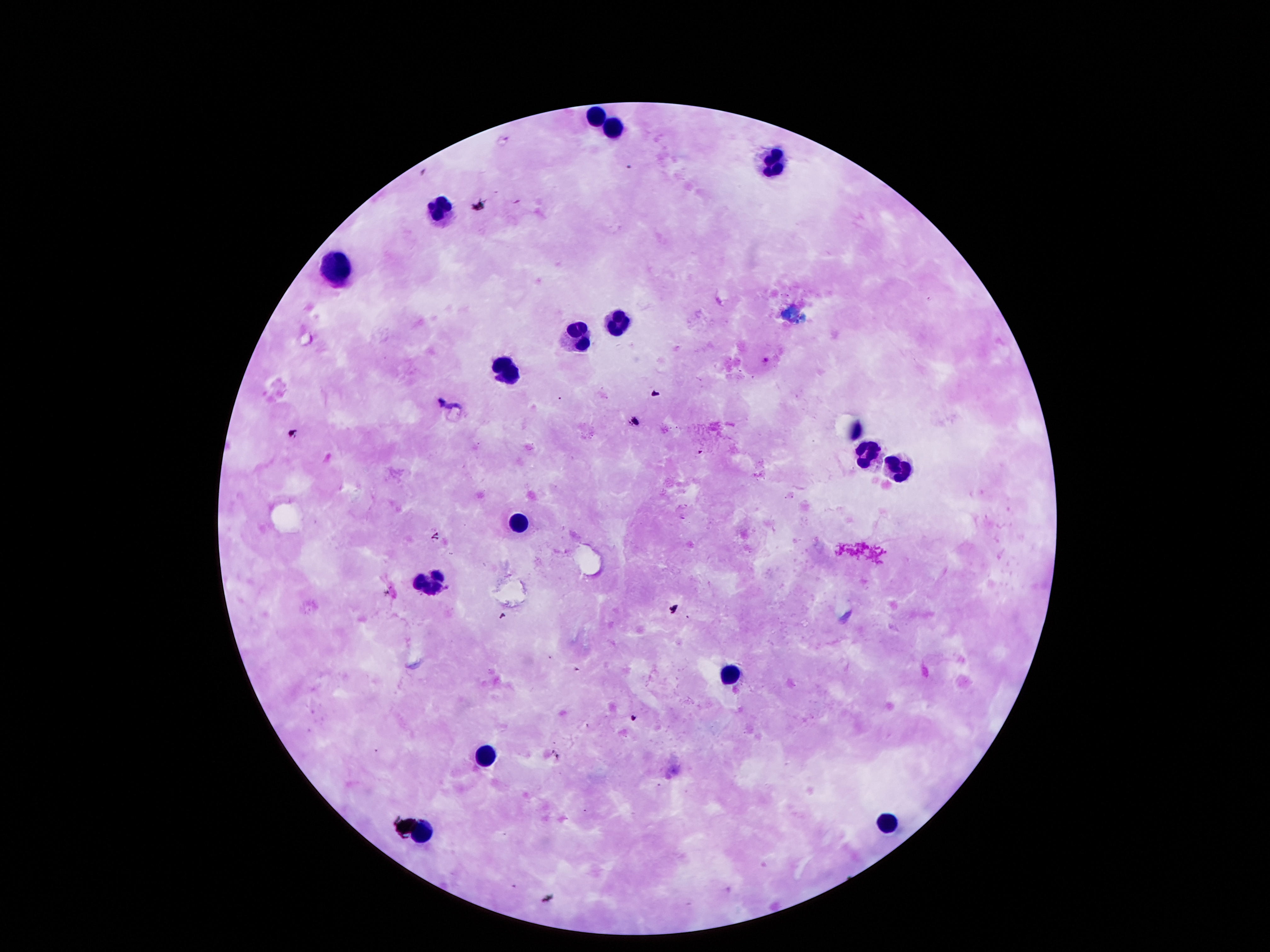
Approximate centers as {x, y} in pixels.
Summary:
  - Leukocyte locations: {593, 113}, {613, 127}, {778, 162}, {440, 211}, {338, 267}, {617, 322}, {577, 335}, {506, 372}, {862, 452}, {898, 465}, {520, 523}, {425, 582}, {732, 671}, {480, 760}, {889, 824}, {422, 833}
  - Field of view: single
  - Stain: Giemsa
  - Preparation: thick peripheral-blood smear
  - Image size: 1270×952 pixels
  - Magnification: 100x
  - Patient malaria status: not infected
  - Capture: smartphone camera through the microscope eyepiece